Classify this cell by malaria status.
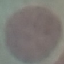
Uninfected.

Summary:
  - Preparation: thin blood smear
  - Capture: smartphone through the microscope eyepiece
  - Stain: Giemsa
  - Image type: automatically extracted cell patch, resized to 64 × 64 pixels